State the blood parasite species.
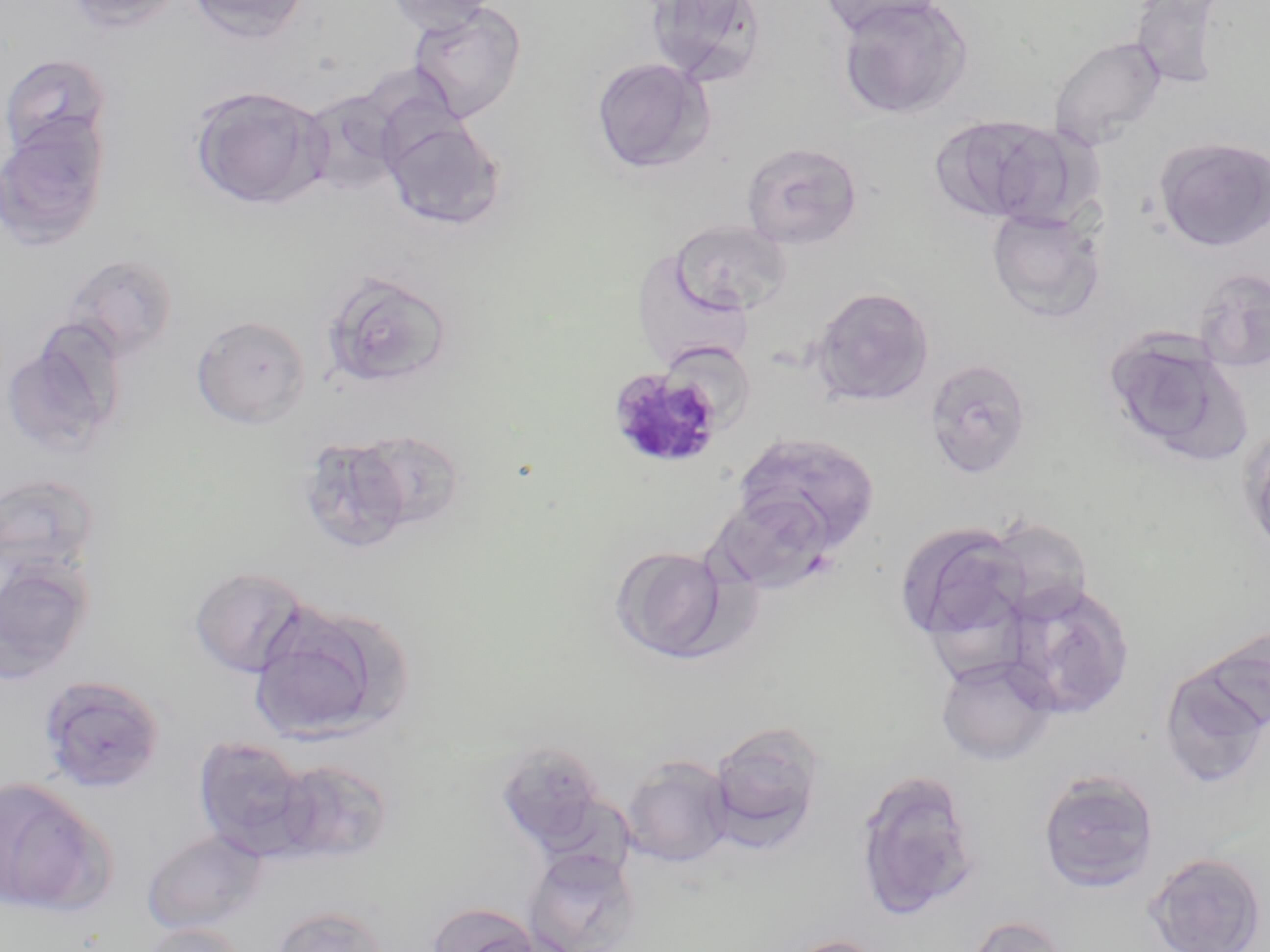

Plasmodium malariae.

Approximate bounding boxes as named x1/y1/x2/y2 corners in pixels. Plasmodium malariae-infected red blood cell locations: (x1=606, y1=366, x2=725, y2=470). Uninfected red blood cell locations: (x1=65, y1=0, x2=185, y2=33), (x1=186, y1=0, x2=311, y2=43), (x1=384, y1=0, x2=497, y2=34), (x1=818, y1=0, x2=946, y2=37), (x1=834, y1=0, x2=973, y2=119), (x1=1128, y1=0, x2=1227, y2=91), (x1=645, y1=1, x2=768, y2=88), (x1=408, y1=2, x2=528, y2=124), (x1=1049, y1=35, x2=1167, y2=150), (x1=1, y1=53, x2=111, y2=159), (x1=590, y1=57, x2=714, y2=175), (x1=188, y1=85, x2=330, y2=209), (x1=297, y1=88, x2=406, y2=198), (x1=381, y1=113, x2=506, y2=231), (x1=931, y1=113, x2=1080, y2=227), (x1=0, y1=117, x2=110, y2=251), (x1=1155, y1=137, x2=1270, y2=251), (x1=741, y1=141, x2=863, y2=249), (x1=985, y1=208, x2=1104, y2=322), (x1=671, y1=220, x2=791, y2=315), (x1=61, y1=253, x2=179, y2=363), (x1=1194, y1=267, x2=1270, y2=372), (x1=320, y1=270, x2=453, y2=390), (x1=811, y1=286, x2=935, y2=407), (x1=191, y1=315, x2=310, y2=428), (x1=1, y1=325, x2=125, y2=459), (x1=1103, y1=329, x2=1248, y2=465), (x1=924, y1=357, x2=1033, y2=479), (x1=352, y1=428, x2=466, y2=533), (x1=732, y1=432, x2=881, y2=558), (x1=298, y1=437, x2=413, y2=554), (x1=0, y1=472, x2=101, y2=583), (x1=708, y1=490, x2=839, y2=594), (x1=610, y1=545, x2=733, y2=662), (x1=0, y1=559, x2=94, y2=684), (x1=190, y1=566, x2=310, y2=677), (x1=1003, y1=579, x2=1135, y2=719), (x1=248, y1=601, x2=409, y2=744), (x1=1201, y1=622, x2=1269, y2=733), (x1=936, y1=655, x2=1057, y2=765), (x1=1159, y1=663, x2=1268, y2=787), (x1=38, y1=675, x2=166, y2=794), (x1=708, y1=722, x2=825, y2=850), (x1=192, y1=735, x2=313, y2=859), (x1=494, y1=741, x2=607, y2=849), (x1=621, y1=755, x2=735, y2=867), (x1=275, y1=758, x2=394, y2=864), (x1=854, y1=769, x2=980, y2=919), (x1=1037, y1=769, x2=1160, y2=893), (x1=0, y1=776, x2=111, y2=916), (x1=142, y1=829, x2=269, y2=933), (x1=523, y1=848, x2=640, y2=952), (x1=1144, y1=852, x2=1267, y2=952), (x1=427, y1=901, x2=543, y2=952), (x1=271, y1=906, x2=389, y2=952), (x1=963, y1=914, x2=1072, y2=952), (x1=138, y1=923, x2=247, y2=952), (x1=784, y1=935, x2=886, y2=952). May-Grünwald-Giemsa-stained preparation. Image is 1270×952 pixels. Thin blood film. Optical microscopy. 1000x magnification. Single field of view.